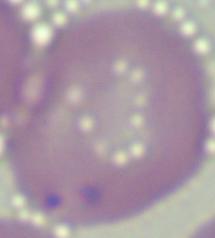
Summary:
  - Identification: Babesia
  - Magnification: 1000x
  - Modality: micrograph